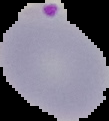

Segmented cell region on a black background. Image is 109×121 pixels. From a thin blood smear. Result: Plasmodium parasites identified.